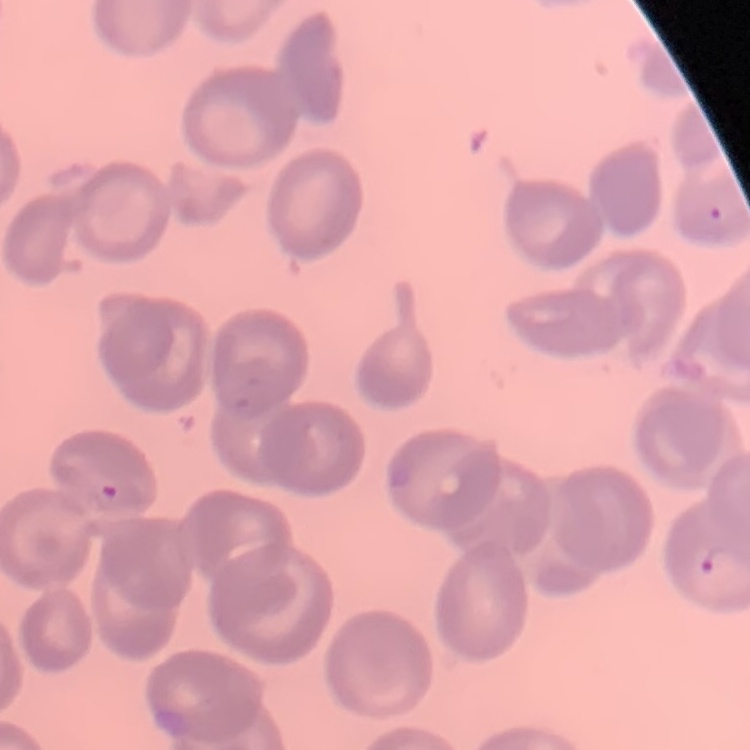

Summary:
  - Erythrocyte morphology: no rouleaux formation
  - Image type: square crop of a larger photomicrograph
  - Preparation: thin blood smear
  - Stain: Field's or Giemsa